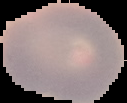 Segmented cell region on a black background. Malaria status: uninfected. From a thin blood film. Image is 127×103 pixels.